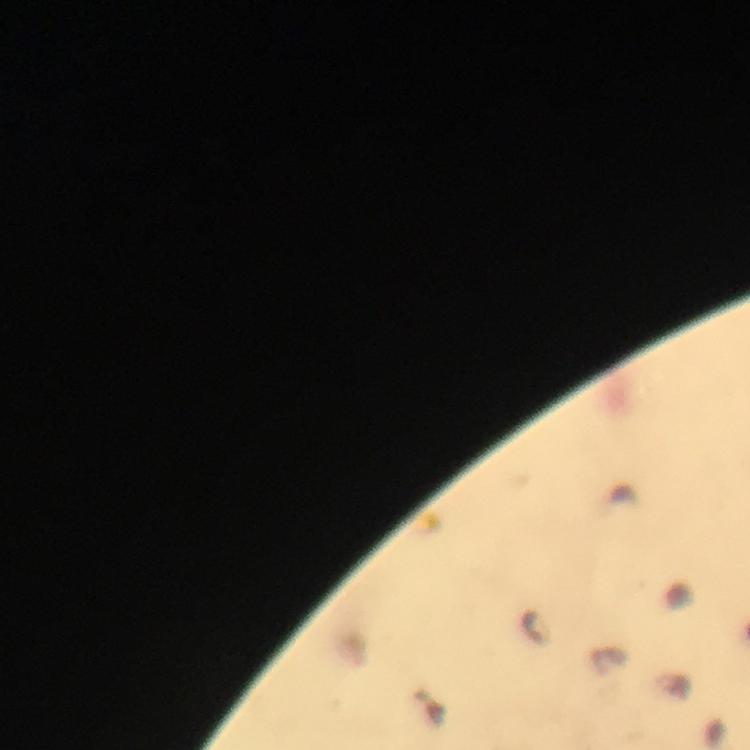

Approximate centers as (x, y) in pixels.
Summary:
  - Malaria parasite locations: (534, 627)
  - Stain: Giemsa
  - Cropped from: a single field of view
  - Magnification: 100x
  - Immersion oil: applied
  - Context: from a diagnostic examination for malaria
  - Preparation: thick smear
  - Capture: smartphone mounted on the microscope
  - Image size: 750×750 pixels